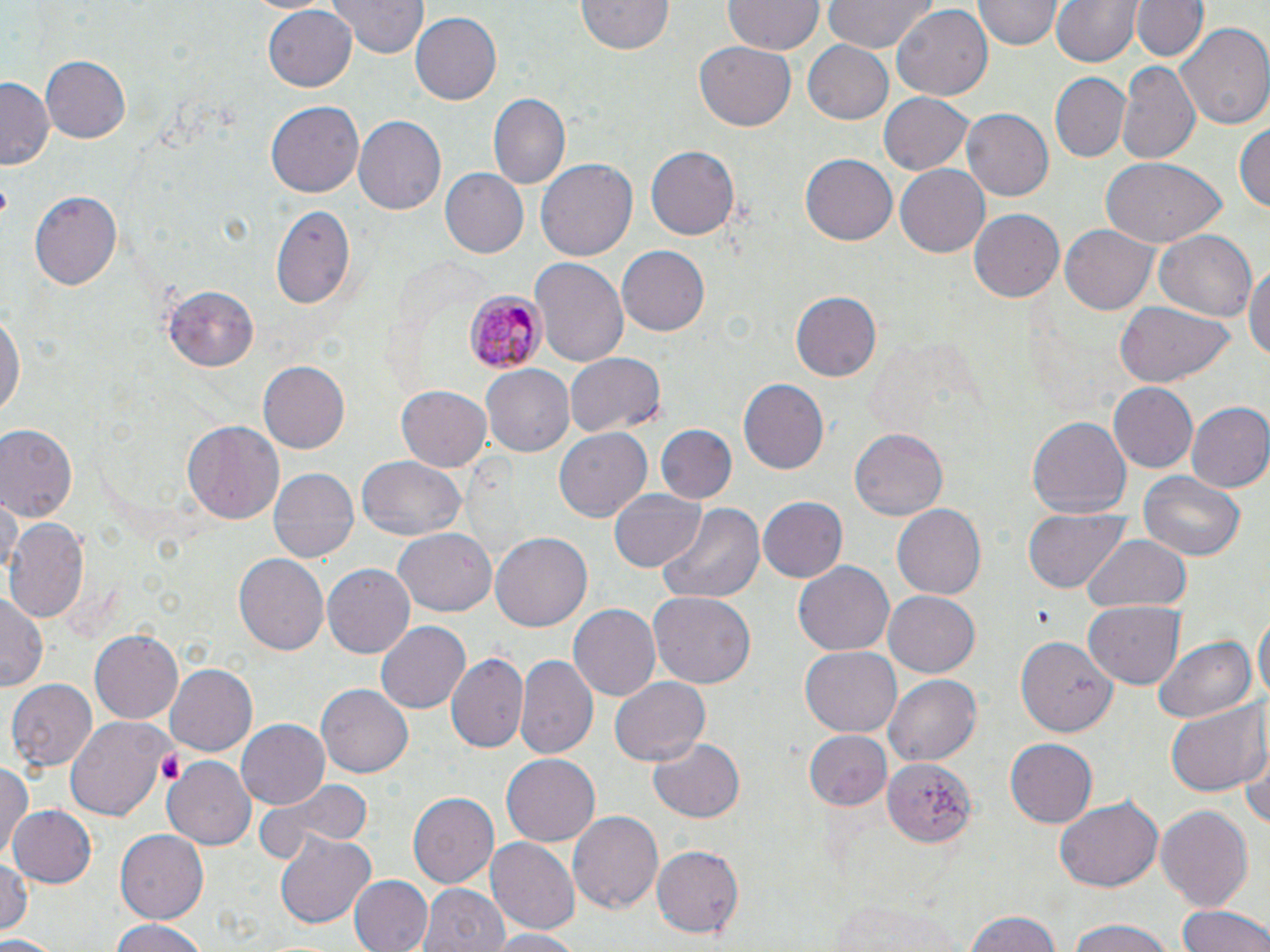

Approximate bounding boxes as (x1, y1, x2, y2) in pixels. Uninfected red blood cell locations: (328, 0, 430, 58), (577, 0, 676, 56), (724, 0, 823, 56), (823, 0, 938, 52), (1053, 0, 1140, 68), (1129, 0, 1211, 64), (974, 1, 1060, 51), (263, 3, 356, 89), (893, 5, 992, 100), (409, 12, 500, 105), (1176, 22, 1270, 131), (802, 39, 894, 124), (695, 43, 795, 132), (40, 55, 133, 144), (1117, 63, 1199, 163), (1048, 73, 1129, 164), (0, 79, 53, 171), (488, 92, 571, 189), (879, 92, 975, 175), (266, 101, 364, 197), (961, 108, 1052, 202), (354, 117, 446, 214), (1235, 120, 1269, 215), (645, 146, 740, 239), (799, 153, 897, 246), (536, 157, 638, 262), (1100, 159, 1225, 246), (896, 164, 989, 257), (439, 169, 528, 259), (29, 191, 121, 291), (271, 206, 355, 309), (968, 206, 1067, 302), (1060, 225, 1160, 313), (1152, 231, 1257, 321), (615, 246, 710, 336), (530, 257, 629, 371), (1245, 259, 1270, 373), (164, 285, 259, 368), (790, 290, 882, 380), (0, 299, 26, 425), (1115, 301, 1232, 386), (564, 353, 666, 437), (258, 361, 349, 455), (482, 366, 575, 457), (738, 378, 829, 475), (1106, 382, 1197, 473), (396, 385, 491, 471), (1185, 402, 1270, 493), (1027, 416, 1131, 520), (183, 420, 284, 527), (656, 425, 735, 505), (0, 426, 77, 522), (553, 428, 650, 523), (850, 428, 946, 522), (355, 456, 466, 540), (266, 469, 359, 565), (1138, 473, 1246, 562), (611, 486, 705, 571), (2, 492, 20, 585), (756, 495, 846, 584), (654, 503, 763, 607), (893, 505, 985, 598), (1024, 509, 1132, 594), (5, 517, 88, 621), (392, 525, 498, 618), (490, 532, 592, 633), (1083, 534, 1192, 616), (232, 551, 328, 654), (794, 560, 895, 657), (322, 564, 416, 659), (647, 590, 758, 690), (885, 591, 980, 677), (0, 592, 44, 690), (1084, 601, 1183, 689), (567, 604, 659, 701), (1254, 607, 1268, 713), (377, 621, 471, 715), (89, 628, 182, 726), (1017, 633, 1120, 738), (1151, 635, 1255, 725), (799, 648, 902, 737), (447, 652, 527, 754), (518, 653, 596, 762), (165, 663, 258, 756), (883, 673, 981, 767), (610, 675, 709, 768), (8, 679, 97, 769), (317, 685, 414, 778), (1164, 701, 1270, 797), (65, 715, 170, 820), (235, 718, 330, 810), (804, 729, 892, 809), (645, 738, 746, 822), (1241, 738, 1270, 837), (1005, 739, 1097, 828), (501, 753, 600, 847), (164, 758, 257, 852), (883, 759, 975, 847), (0, 762, 35, 860), (259, 778, 373, 864), (407, 789, 499, 888), (1056, 798, 1163, 893), (8, 804, 98, 888), (1153, 804, 1254, 912), (567, 810, 664, 915), (116, 830, 208, 922), (274, 831, 376, 930), (486, 838, 578, 935), (651, 844, 745, 938), (0, 857, 31, 936), (348, 875, 431, 952), (420, 884, 508, 952), (827, 899, 967, 952), (1177, 903, 1270, 952), (962, 908, 1065, 952), (107, 919, 211, 952), (1062, 921, 1178, 952), (486, 929, 587, 952), (0, 936, 56, 952). Platelet locations: (1035, 601, 1057, 632), (155, 751, 188, 787). Plasmodium malariae-infected red blood cell locations: (463, 290, 543, 374). Slide-level diagnosis: Plasmodium malariae. Captured at 1000x magnification. Single field of view. Thin blood film. Light microscopy. May-Grünwald-Giemsa stain. Image is 1270×952 pixels.